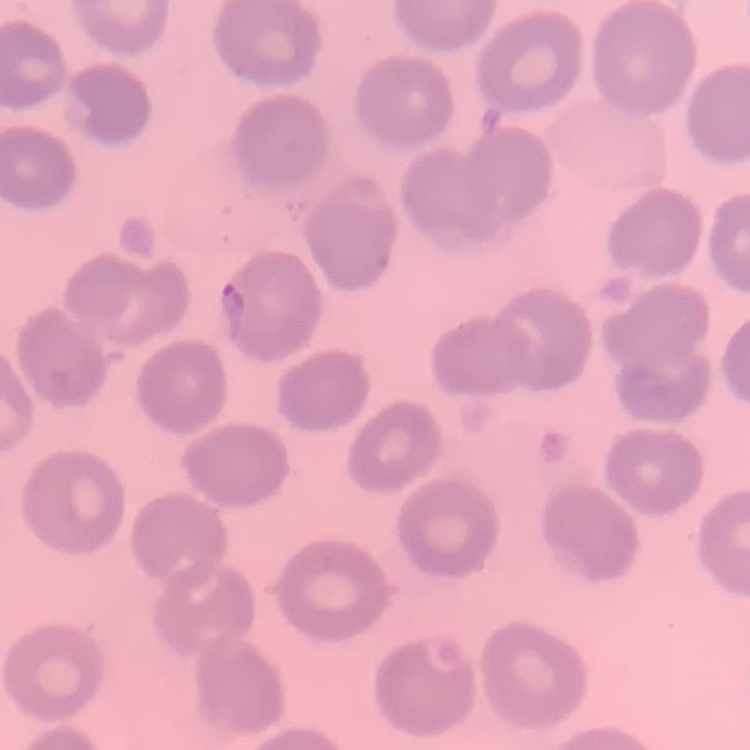

Summary:
  - Red blood cell morphology: no rouleaux formation
  - Image type: one tile cut from a larger photomicrograph
  - Preparation: thin blood smear
  - Stain: Field's or Giemsa